Describe the morphology of the red blood cells.
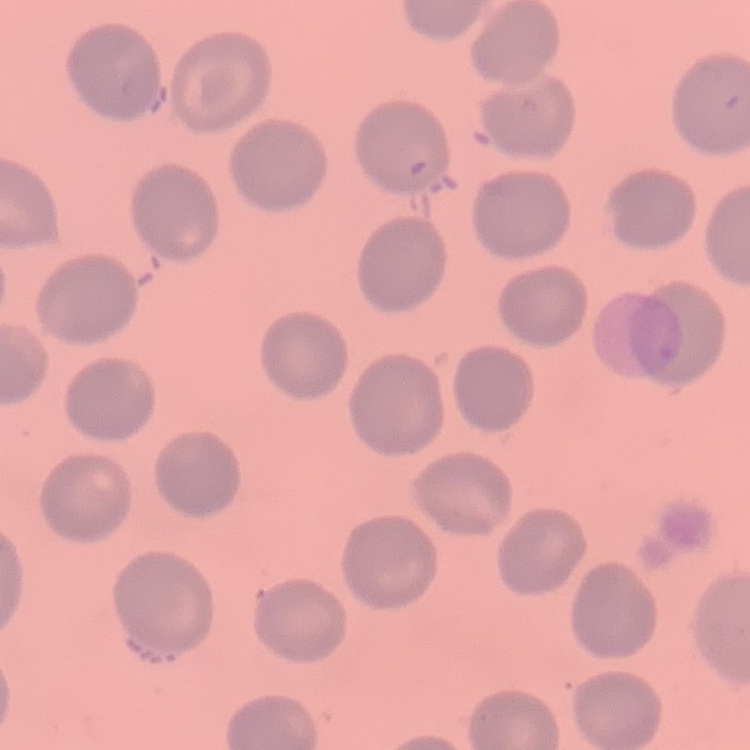

They show no rouleaux formation.

One tile cut from a larger photomicrograph. Thin peripheral smear. Field's or Giemsa stain.